Locate every leukocyte (white blood cell).
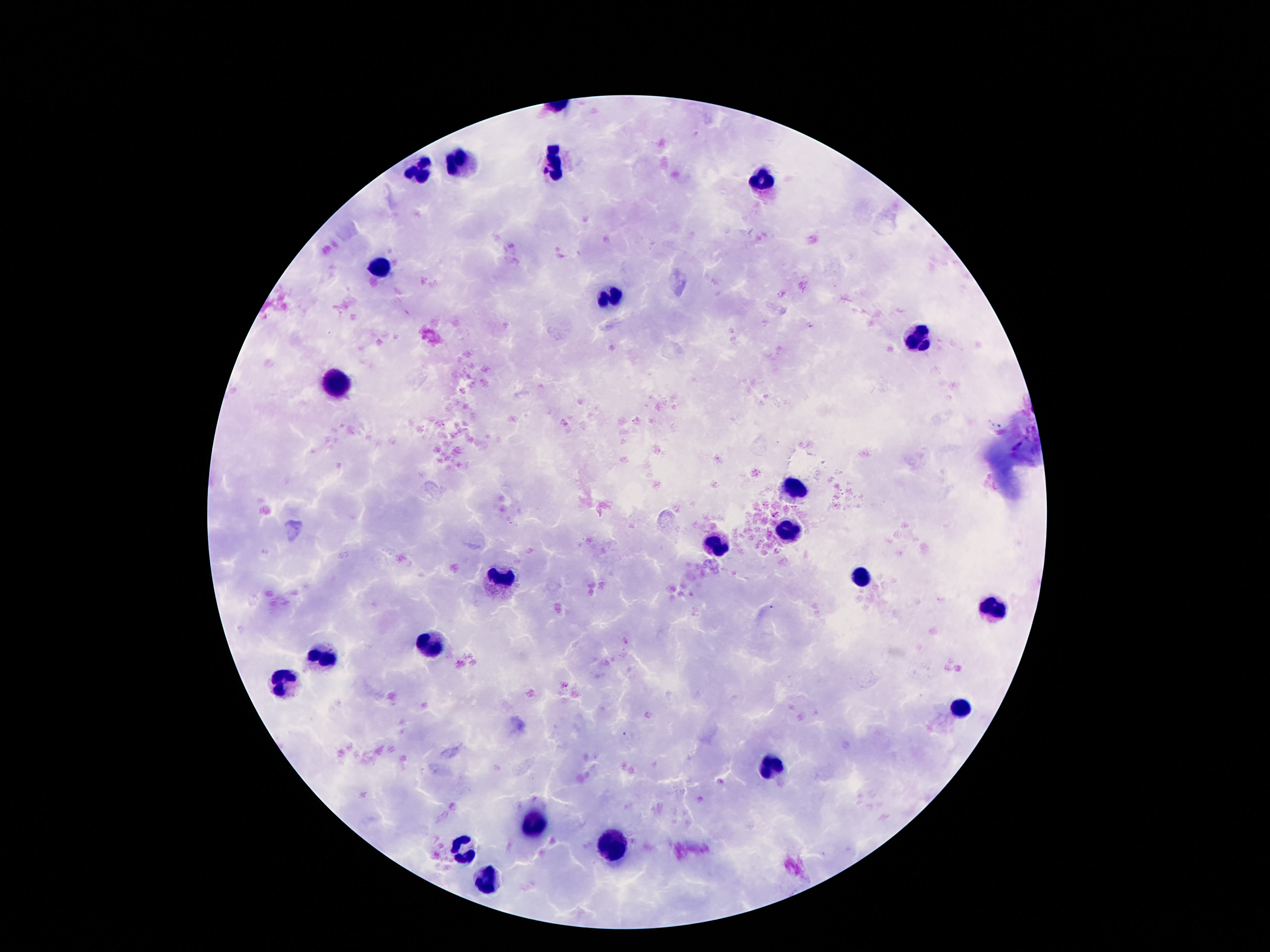
Approximate centers as [x, y] in pixels.
Leukocytes: [556, 161], [457, 164], [421, 168], [761, 177], [376, 268], [610, 301], [918, 336], [341, 383], [791, 486], [789, 529], [714, 544], [503, 577], [860, 579], [994, 611], [429, 643], [320, 660], [289, 680], [964, 706], [770, 768], [531, 820], [462, 850], [612, 850], [488, 880].

One field from this slide. Giemsa stain. Patient malaria status: uninfected. Photographed through the microscope eyepiece with a smartphone camera. 100x magnification. Image is 1270×952 pixels. Thick blood film.